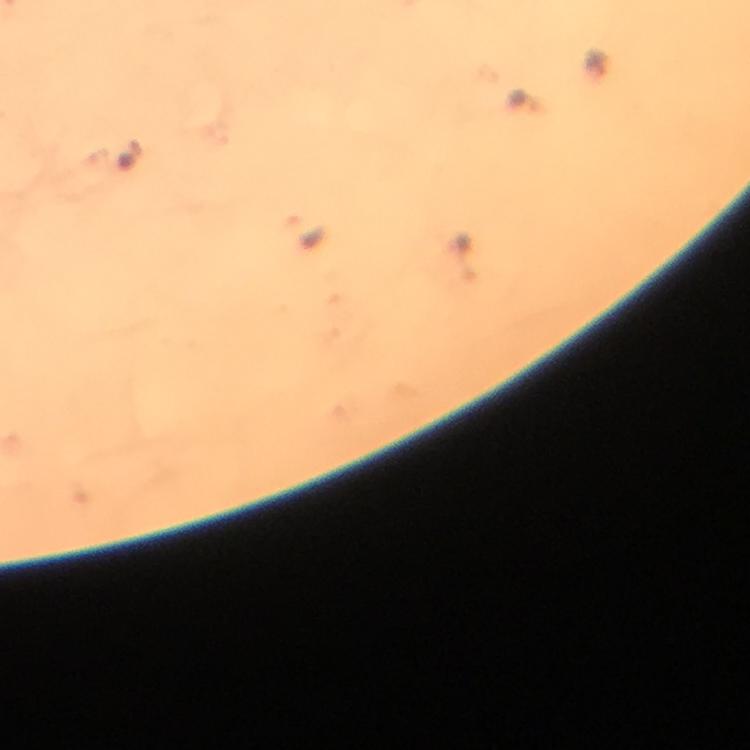
Approximate centers as [x, y] in pixels.
Summary:
  - Plasmodium parasite locations: [129, 156], [306, 231]
  - Preparation: thick blood smear
  - Magnification: 100x
  - Cropped from: a single field of view
  - Stain: Giemsa
  - Capture: smartphone mounted on the microscope
  - Context: from a malaria diagnostic workup
  - Image size: 750×750 pixels
  - Immersion oil: applied